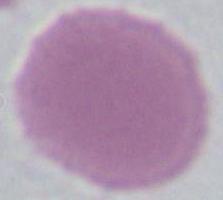
modality: photomicrograph
magnification: 1000x
identification: erythrocyte